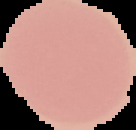

Result: negative for malaria parasites. Image is 136×130 pixels. The area outside the segmented cell region is set to black. From a thin blood smear.